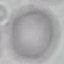
malaria status = uninfected
capture = smartphone through the microscope eyepiece
preparation = thin blood film
image type = cell patch, automatically extracted from a larger field of view and resized to 64 × 64 pixels
stain = Giemsa